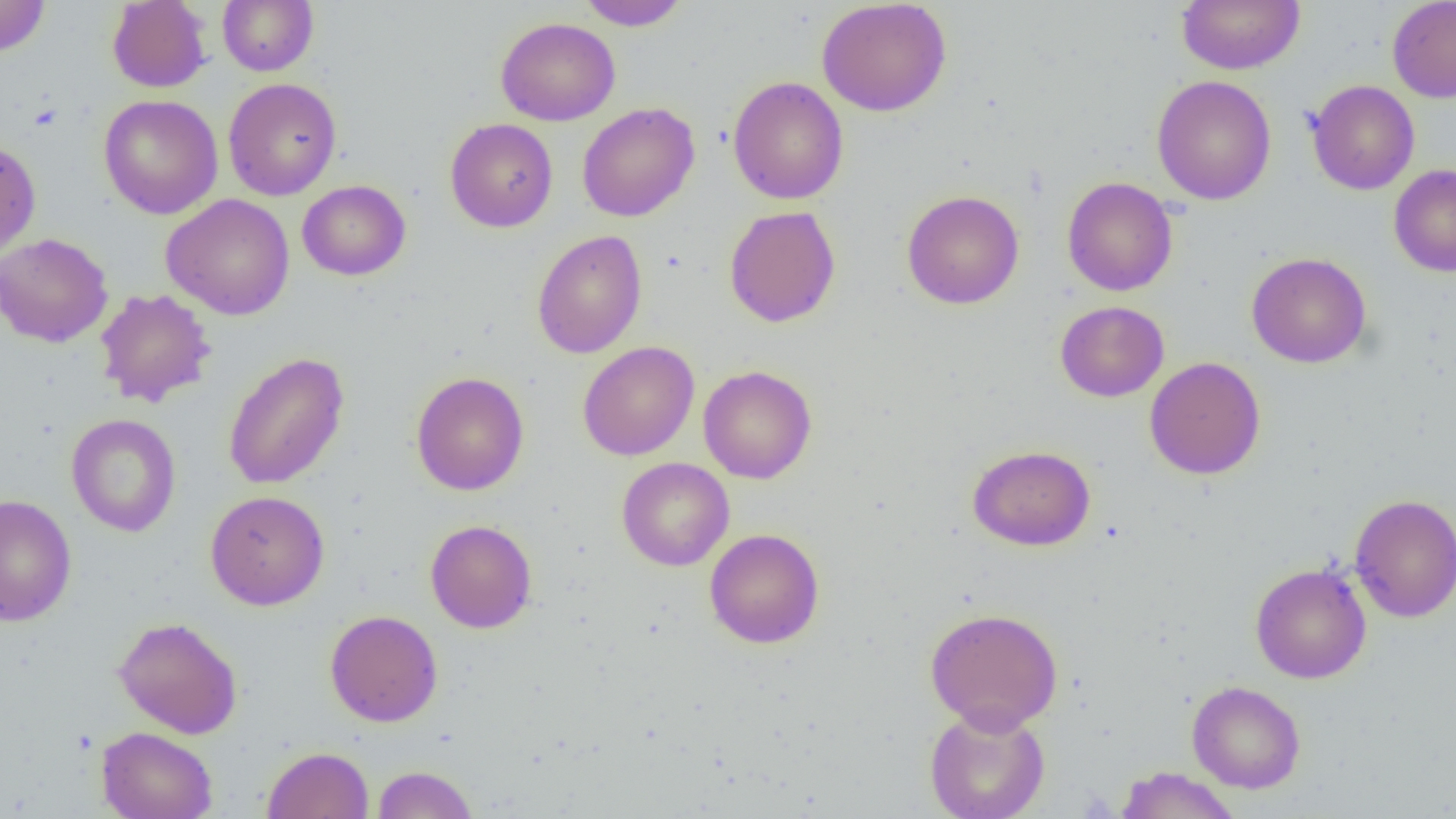
Summary:
  - Coordinate format: approximate bounding boxes as (x1, y1, x2, y2) in pixels
  - Uninfected red blood cell locations: (0, 0, 51, 57), (217, 0, 318, 76), (816, 0, 953, 117), (1176, 0, 1305, 74), (1387, 0, 1456, 103), (107, 1, 211, 92), (579, 1, 690, 31), (495, 17, 621, 126), (1151, 75, 1277, 205), (728, 76, 848, 205), (223, 77, 342, 200), (1306, 80, 1420, 195), (98, 94, 223, 219), (576, 102, 700, 222), (444, 118, 558, 232), (0, 141, 41, 261), (1388, 163, 1456, 277), (1062, 176, 1178, 296), (297, 180, 411, 281), (901, 189, 1024, 309), (160, 194, 295, 320), (723, 205, 841, 327), (532, 230, 647, 359), (0, 232, 113, 348), (1246, 251, 1372, 369), (94, 288, 217, 408), (1055, 300, 1169, 402), (577, 341, 699, 461), (222, 352, 349, 490), (1145, 356, 1266, 480), (698, 365, 817, 484), (411, 371, 529, 496), (66, 413, 181, 537), (967, 444, 1096, 551), (616, 457, 735, 571), (205, 490, 330, 610), (0, 493, 77, 627), (1349, 493, 1456, 622), (425, 520, 537, 633), (704, 529, 824, 649), (1249, 562, 1372, 684), (924, 607, 1064, 732), (324, 610, 443, 727), (113, 617, 243, 739), (1187, 680, 1306, 793), (923, 705, 1051, 819), (96, 726, 217, 819), (262, 746, 373, 819), (371, 765, 478, 818), (1114, 766, 1241, 819)
  - Slide-level diagnosis: no evidence of blood parasites
  - Field of view: one of a larger specimen
  - Preparation: thin blood film
  - Image size: 1456×819 pixels
  - Modality: optical microscopy
  - Magnification: 1000x